Assess this cell for malaria.
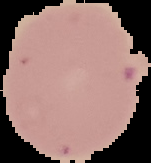

Uninfected.

Segmented cell region on a black background. From a thin blood film. Image is 151×163 pixels.